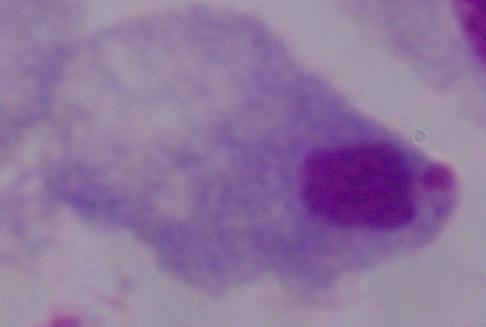

Photomicrograph. A trichomonad is seen. 1000x magnification.